Give the extent of all Plasmodium falciparum-infected red blood cells.
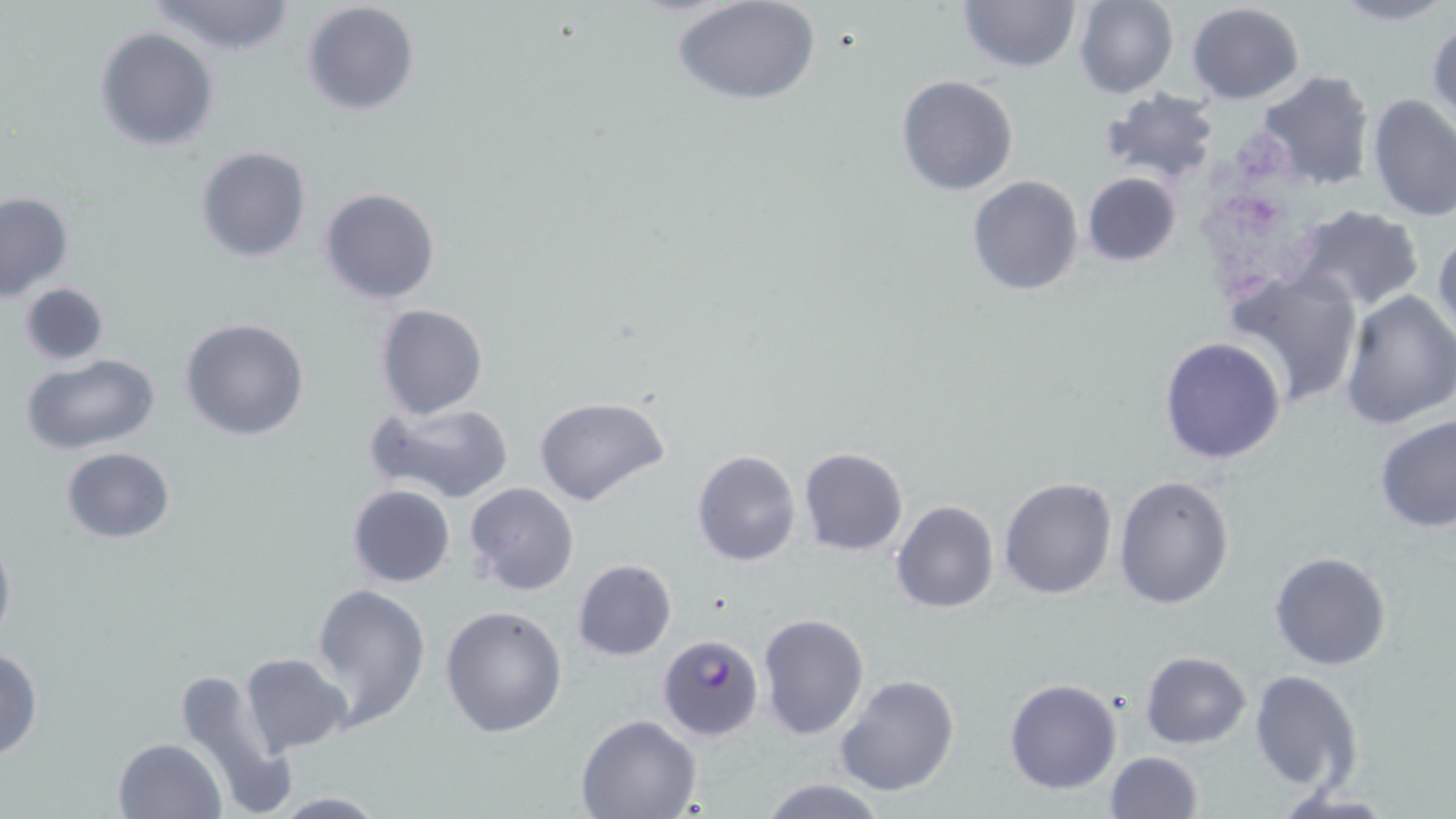
Approximate bounding boxes as [x1, y1, x2, y2] in pixels.
Plasmodium falciparum-infected red blood cells: [657, 632, 765, 741].

slide-level diagnosis = Plasmodium falciparum
uninfected red blood cell locations = approximate bounding boxes as [x1, y1, x2, y2] in pixels: [674, 0, 823, 107], [956, 0, 1081, 72], [1073, 0, 1178, 99], [1330, 0, 1456, 27], [145, 1, 299, 57], [301, 2, 419, 118], [1186, 2, 1305, 105], [1426, 17, 1455, 126], [93, 26, 218, 151], [1255, 70, 1375, 193], [895, 74, 1018, 195], [1099, 89, 1221, 186], [1365, 94, 1456, 225], [195, 146, 310, 263], [1081, 172, 1184, 269], [967, 175, 1084, 296], [318, 187, 441, 305], [0, 192, 74, 301], [1289, 204, 1427, 312], [1431, 226, 1456, 345], [1227, 269, 1365, 408], [18, 282, 111, 365], [1337, 289, 1456, 432], [373, 303, 488, 420], [180, 318, 310, 441], [1159, 335, 1288, 465], [23, 354, 161, 455], [535, 395, 669, 507], [368, 402, 516, 504], [1373, 413, 1455, 533], [60, 447, 177, 544], [798, 447, 909, 558], [692, 450, 802, 566], [1113, 475, 1235, 611], [997, 476, 1118, 600], [346, 484, 456, 588], [464, 484, 580, 597], [892, 500, 998, 614], [0, 531, 15, 650], [1268, 550, 1392, 671], [572, 557, 676, 660], [311, 583, 431, 727], [440, 604, 568, 738], [757, 611, 869, 741], [0, 649, 43, 761], [1140, 651, 1251, 749], [239, 652, 352, 756], [173, 667, 295, 816], [1249, 669, 1364, 792], [834, 674, 960, 798], [1004, 678, 1122, 795], [577, 714, 703, 818], [113, 737, 224, 818], [1105, 751, 1203, 819], [755, 777, 888, 818], [1269, 789, 1400, 817], [262, 791, 391, 817]
platelet locations = approximate bounding boxes as [x1, y1, x2, y2] in pixels: [1235, 131, 1288, 184], [1205, 178, 1287, 244], [1209, 245, 1280, 295]
magnification = 1000x
field of view = one of a larger specimen
stain = May-Grünwald-Giemsa
image size = 1456×819 pixels
preparation = thin blood film
modality = light microscopy